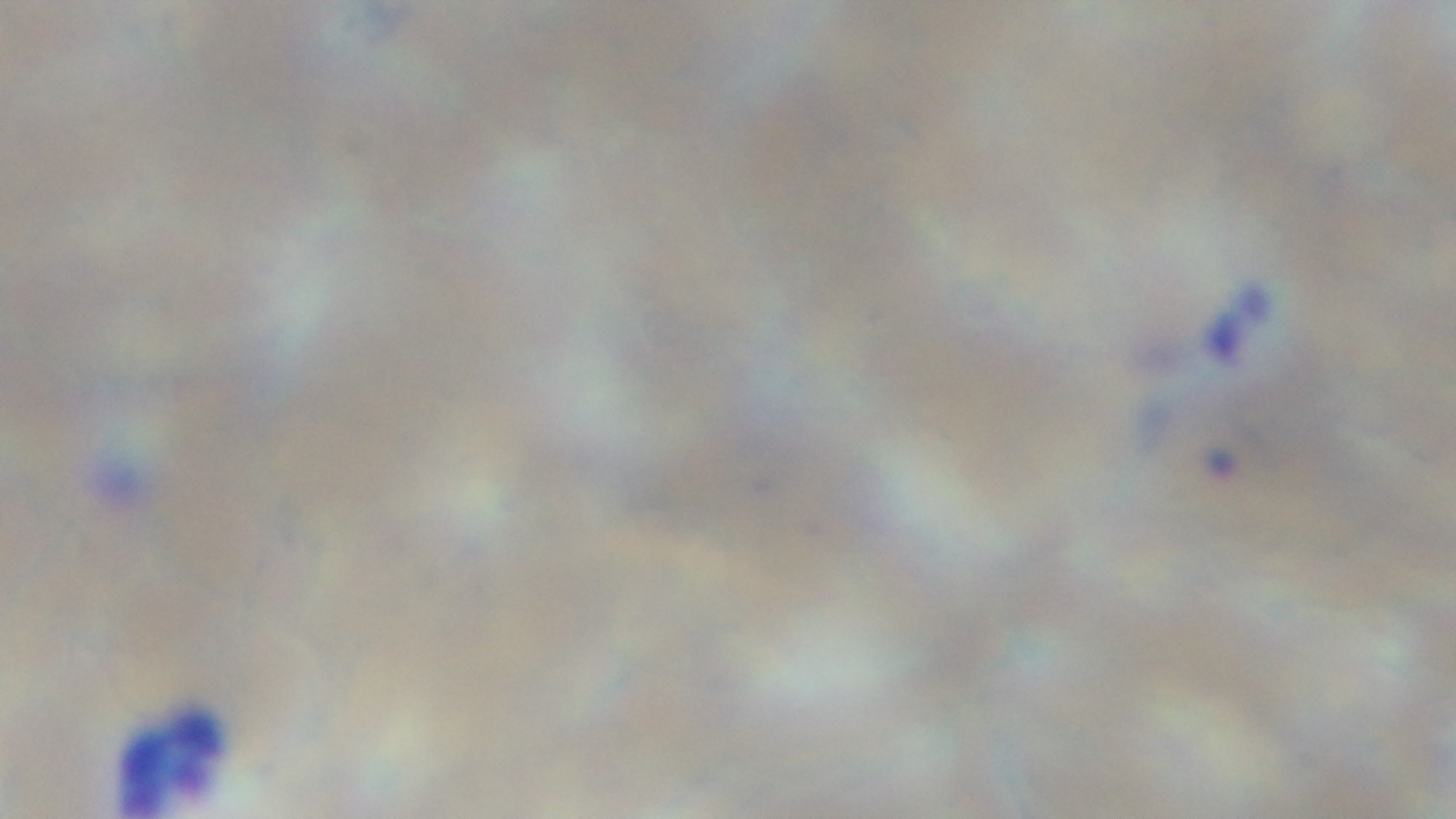

Summary:
  - Field of view: single
  - Stain: Giemsa
  - Preparation: thin smear
  - Modality: light microscopy
  - Objective: 100x oil immersion
  - Capture: mounted 4K digital camera
  - Malaria status: infected